Assess the morphology of the red blood cells.
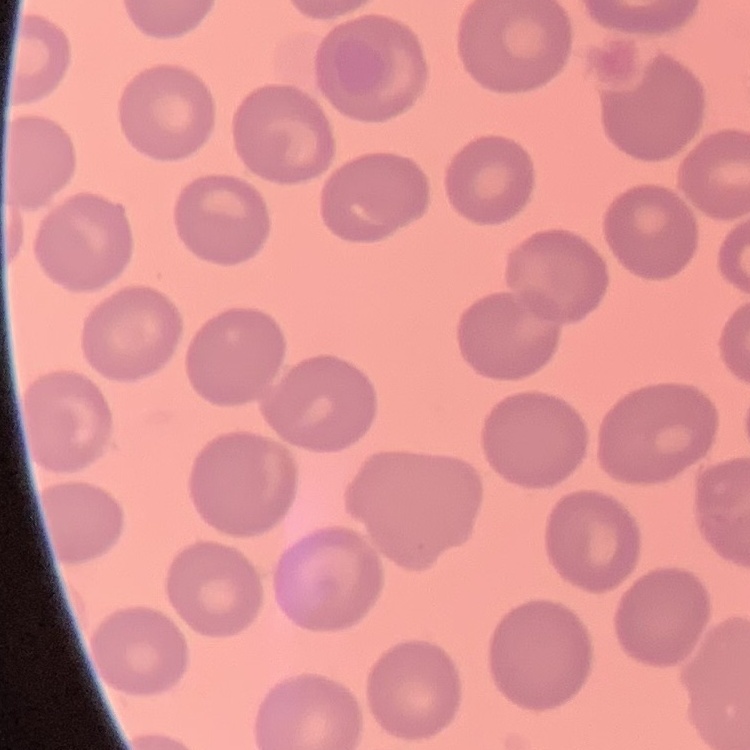
They show no rouleaux formation.

stain = Field's or Giemsa
image type = one tile cut from a larger photomicrograph
preparation = thin peripheral smear